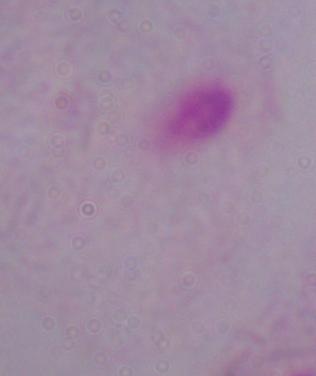

Micrograph. Captured at 1000x magnification. A trichomonad is shown.